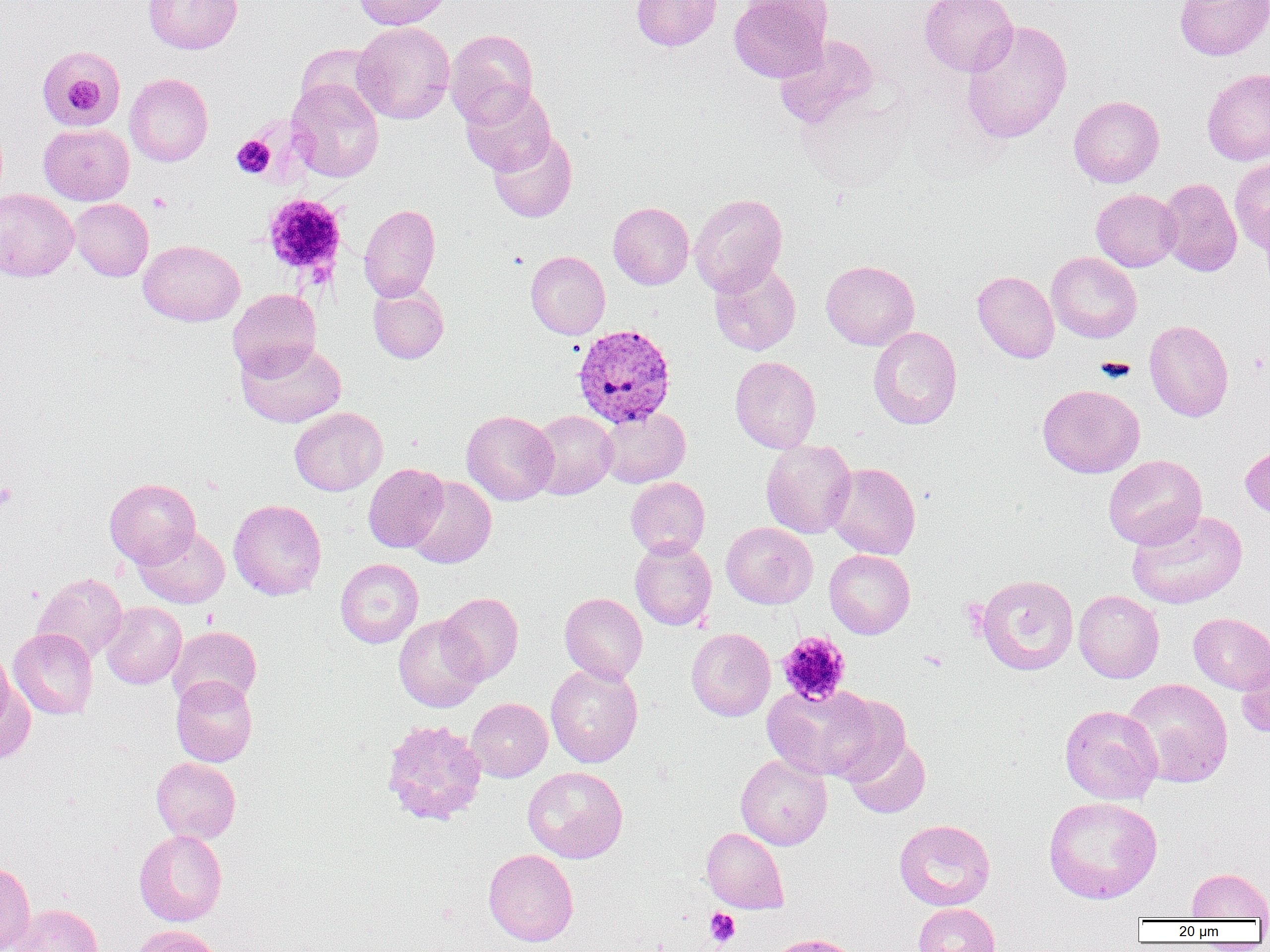

Summary:
  - Coordinate format: approximate bounding boxes as [x1, y1, x2, y2] in pixels
  - Uninfected red blood cell locations: [143, 0, 242, 54], [353, 0, 452, 29], [631, 0, 722, 51], [729, 0, 832, 82], [919, 0, 1018, 76], [1174, 0, 1270, 61], [960, 19, 1073, 144], [353, 22, 455, 123], [445, 29, 538, 127], [774, 35, 878, 129], [293, 42, 385, 123], [36, 51, 128, 132], [1201, 68, 1270, 166], [124, 73, 213, 166], [287, 77, 384, 183], [460, 84, 556, 176], [1068, 95, 1165, 187], [39, 124, 134, 205], [488, 130, 577, 222], [1229, 157, 1270, 254], [1157, 178, 1242, 276], [0, 188, 79, 281], [1091, 188, 1182, 272], [689, 193, 788, 296], [70, 199, 153, 281], [608, 201, 694, 290], [359, 204, 441, 301], [138, 240, 244, 327], [526, 251, 610, 339], [1046, 251, 1142, 343], [821, 260, 919, 350], [709, 262, 801, 356], [972, 270, 1059, 363], [368, 283, 449, 363], [228, 289, 321, 379], [1144, 319, 1234, 422], [868, 327, 962, 429], [236, 338, 346, 428], [730, 356, 821, 453], [1037, 384, 1145, 477], [289, 407, 387, 495], [598, 407, 690, 487], [461, 410, 558, 505], [527, 410, 617, 499], [760, 439, 856, 539], [1240, 440, 1270, 520], [1104, 454, 1206, 549], [825, 462, 921, 559], [363, 464, 448, 552], [405, 477, 496, 569], [626, 477, 710, 558], [104, 478, 201, 568], [229, 499, 327, 600], [1126, 509, 1247, 609], [721, 522, 817, 608], [134, 527, 230, 608], [630, 538, 717, 630], [824, 549, 915, 639], [335, 558, 423, 648], [34, 572, 127, 663], [976, 574, 1079, 676], [1074, 590, 1164, 683], [437, 592, 523, 684], [560, 593, 647, 684], [101, 602, 186, 689], [1188, 612, 1270, 694], [393, 616, 486, 712], [167, 625, 262, 709], [8, 628, 98, 719], [686, 628, 775, 721], [1236, 644, 1270, 739], [0, 648, 15, 734], [546, 663, 643, 767], [171, 675, 258, 767], [1121, 677, 1233, 788], [0, 681, 35, 764], [762, 683, 884, 781], [824, 694, 907, 783], [466, 698, 552, 781], [1059, 705, 1162, 804], [381, 719, 488, 825], [844, 734, 931, 819], [735, 754, 832, 850], [151, 757, 240, 843], [522, 766, 628, 863], [1043, 796, 1163, 904], [894, 819, 995, 910], [702, 827, 789, 913], [134, 829, 227, 926], [483, 849, 578, 946], [0, 861, 35, 952], [1186, 868, 1270, 920], [8, 903, 103, 952], [913, 903, 1000, 952], [128, 924, 221, 952], [766, 933, 860, 952]
  - Platelet locations: [55, 58, 111, 122], [231, 135, 275, 178], [148, 192, 172, 213], [262, 194, 347, 278], [0, 482, 16, 509], [777, 632, 851, 705], [918, 650, 948, 672], [705, 908, 741, 947]
  - Plasmodium vivax-infected red blood cell locations: [573, 323, 677, 427]
  - Slide-level diagnosis: Plasmodium vivax
  - Preparation: thin blood smear
  - Magnification: 1000x
  - Field of view: one of a larger specimen
  - Image size: 1270×952 pixels
  - Modality: optical microscopy